Classify this cell by malaria status.
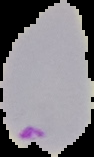
Parasitized.

preparation = thin blood smear
image type = cell region segmented out of the field of view; surrounding area masked to black
image size = 94×157 pixels